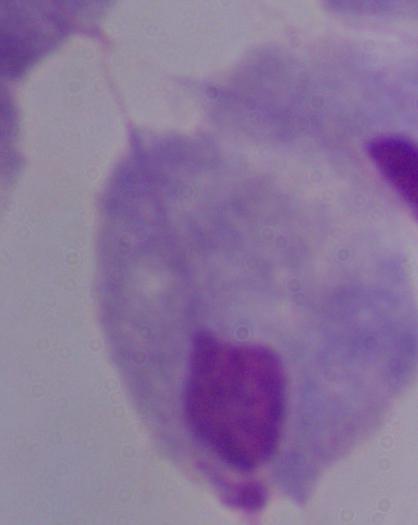

Summary:
  - Modality: photomicrograph
  - Magnification: 1000x
  - Identification: trichomonad